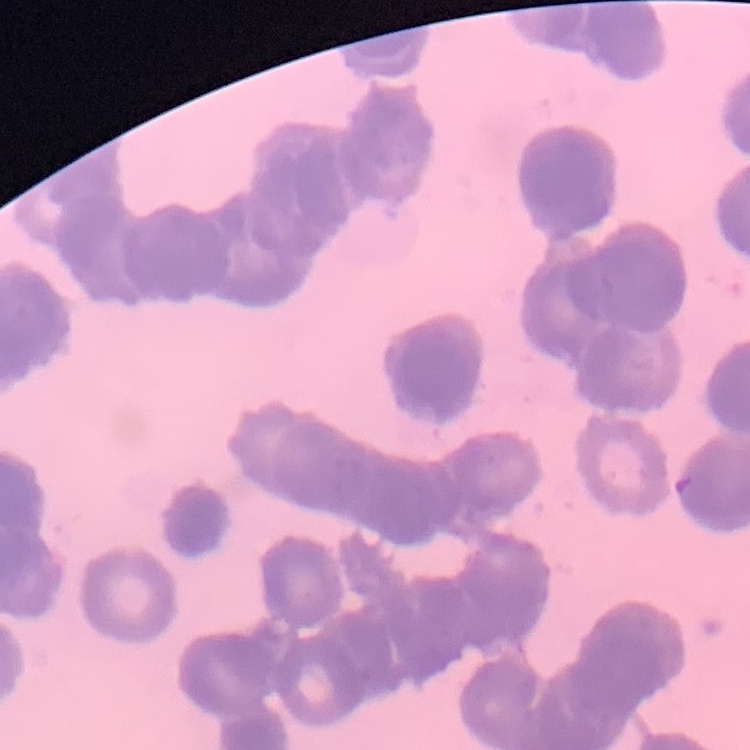

Summary:
  - Red blood cell morphology: rouleaux formation
  - Stain: Field's or Giemsa
  - Preparation: thin blood smear
  - Image type: square crop of a larger photomicrograph